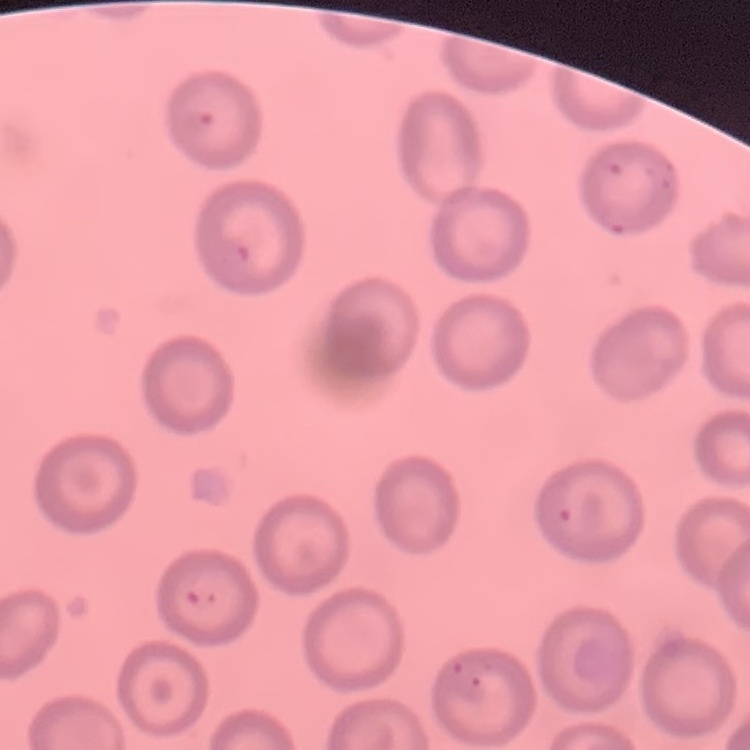 The erythrocytes exhibit no rouleaux formation. One tile cut from a larger photomicrograph. Field's or Giemsa stain. Thin blood film.